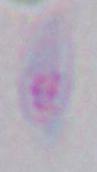
Toxoplasma gondii is shown. 1000x magnification. Photomicrograph.